Name the blood parasite species.
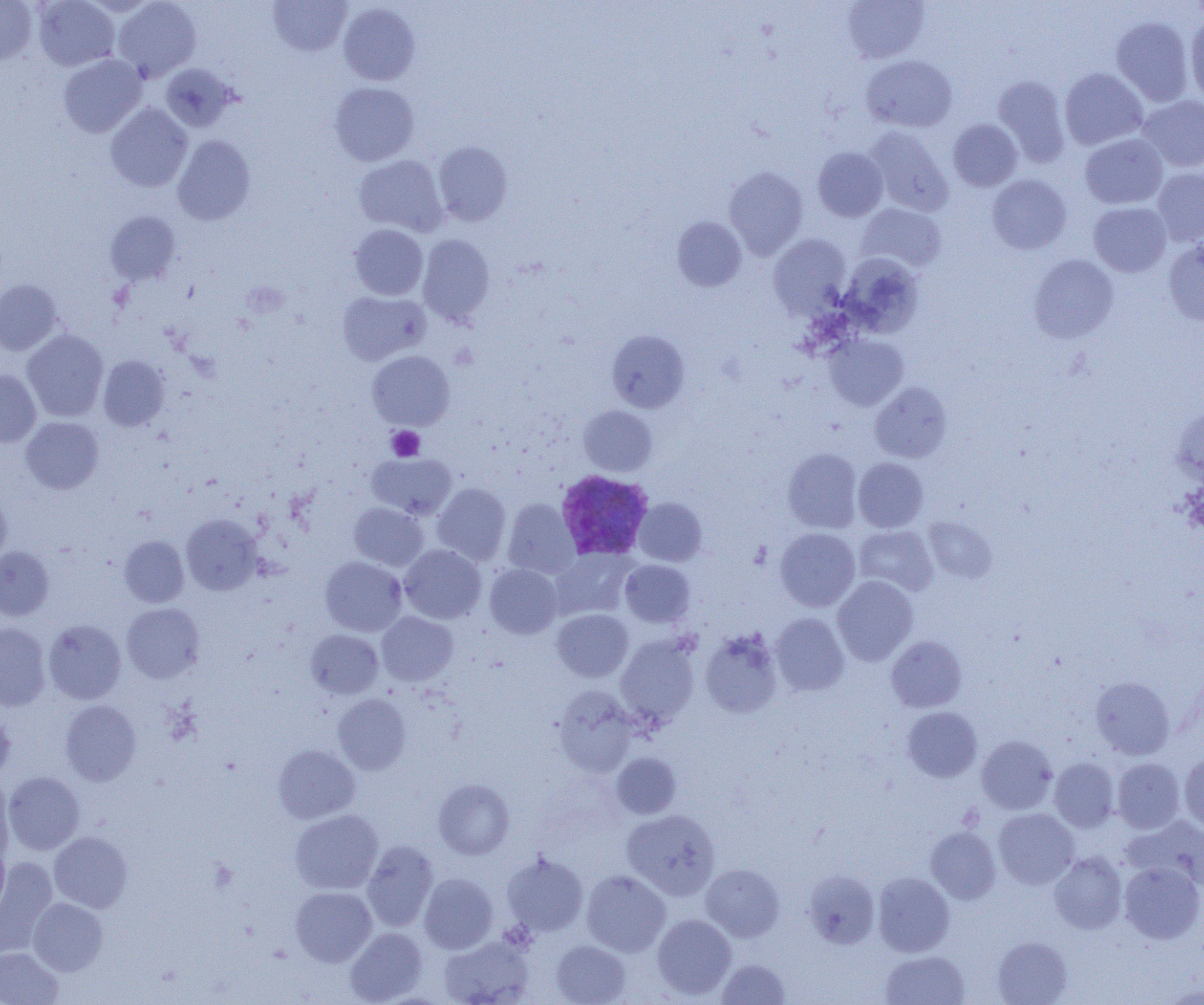
Plasmodium vivax.

Approximate bounding boxes as [x1, y1, x2, y2] in pixels. Plasmodium vivax-infected red blood cell locations: [555, 469, 654, 560]. Uninfected red blood cell locations: [0, 0, 36, 65], [33, 0, 119, 71], [112, 0, 201, 82], [268, 0, 351, 56], [842, 0, 930, 63], [339, 3, 419, 85], [1185, 15, 1204, 104], [1111, 16, 1194, 107], [58, 54, 146, 137], [861, 55, 957, 133], [161, 63, 239, 132], [1059, 68, 1147, 150], [993, 75, 1071, 167], [329, 82, 419, 166], [1137, 95, 1204, 172], [106, 103, 192, 192], [948, 119, 1022, 191], [865, 126, 953, 216], [1080, 134, 1168, 209], [173, 135, 255, 226], [434, 141, 512, 226], [813, 147, 888, 221], [354, 155, 448, 236], [724, 166, 807, 258], [1153, 167, 1204, 246], [987, 174, 1071, 254], [1088, 202, 1171, 277], [856, 203, 946, 273], [105, 211, 181, 285], [672, 216, 746, 292], [350, 224, 428, 300], [417, 234, 495, 326], [768, 234, 850, 317], [1163, 238, 1204, 326], [838, 254, 923, 338], [1029, 254, 1119, 343], [0, 279, 61, 355], [337, 291, 429, 365], [607, 329, 690, 412], [22, 330, 109, 422], [823, 334, 908, 411], [367, 350, 454, 430], [98, 355, 169, 431], [0, 369, 41, 447], [870, 382, 952, 463], [1171, 404, 1204, 486], [578, 405, 657, 476], [21, 417, 103, 494], [782, 447, 863, 533], [367, 453, 457, 519], [853, 457, 928, 532], [432, 483, 511, 565], [0, 489, 11, 567], [633, 498, 706, 566], [503, 499, 580, 578], [349, 502, 427, 571], [181, 514, 262, 595], [924, 517, 997, 582], [854, 525, 938, 596], [775, 528, 860, 611], [119, 536, 189, 607], [400, 544, 486, 624], [0, 546, 53, 620], [551, 549, 635, 619], [320, 557, 407, 636], [620, 559, 695, 627], [484, 564, 562, 639], [832, 575, 918, 665], [122, 603, 204, 683], [552, 609, 633, 682], [377, 611, 458, 686], [771, 613, 849, 696], [44, 619, 126, 704], [0, 623, 50, 711], [699, 629, 783, 718], [305, 630, 383, 699], [615, 635, 699, 727], [886, 635, 966, 712], [1091, 676, 1174, 759], [554, 686, 637, 776], [333, 693, 411, 775], [60, 700, 141, 785], [0, 706, 15, 783], [902, 706, 982, 782], [976, 735, 1057, 814], [274, 744, 360, 823], [612, 752, 681, 819], [1179, 754, 1204, 831], [1049, 757, 1119, 832], [1112, 758, 1185, 833], [3, 772, 84, 855], [0, 776, 15, 865], [434, 779, 514, 859], [994, 808, 1079, 888], [290, 809, 382, 894], [622, 809, 720, 900], [1122, 816, 1204, 890], [926, 826, 1001, 904], [49, 831, 132, 913], [0, 840, 10, 916], [362, 840, 438, 931], [502, 852, 588, 936], [1049, 852, 1127, 934], [0, 857, 59, 957], [1119, 861, 1204, 943], [701, 864, 784, 942], [581, 870, 671, 956], [804, 870, 879, 949], [873, 872, 954, 957], [419, 873, 498, 954], [291, 886, 377, 966], [28, 897, 108, 975], [652, 914, 736, 1000], [345, 927, 428, 1004], [439, 934, 535, 1005], [992, 936, 1072, 1004], [551, 940, 630, 1005], [0, 947, 63, 1005], [881, 950, 969, 1005], [716, 958, 790, 1004]. Platelet locations: [387, 426, 424, 461]. Light microscopy. Single field of view. Thin blood smear. Image is 1204×1005 pixels. 1000x magnification.